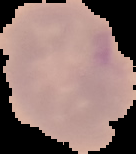

preparation = thin blood film
image size = 136×154 pixels
malaria status = uninfected
image type = cell region segmented out of the field of view; surrounding area masked to black